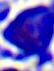

Micrograph. Captured at 400x magnification. A leukocyte is shown.